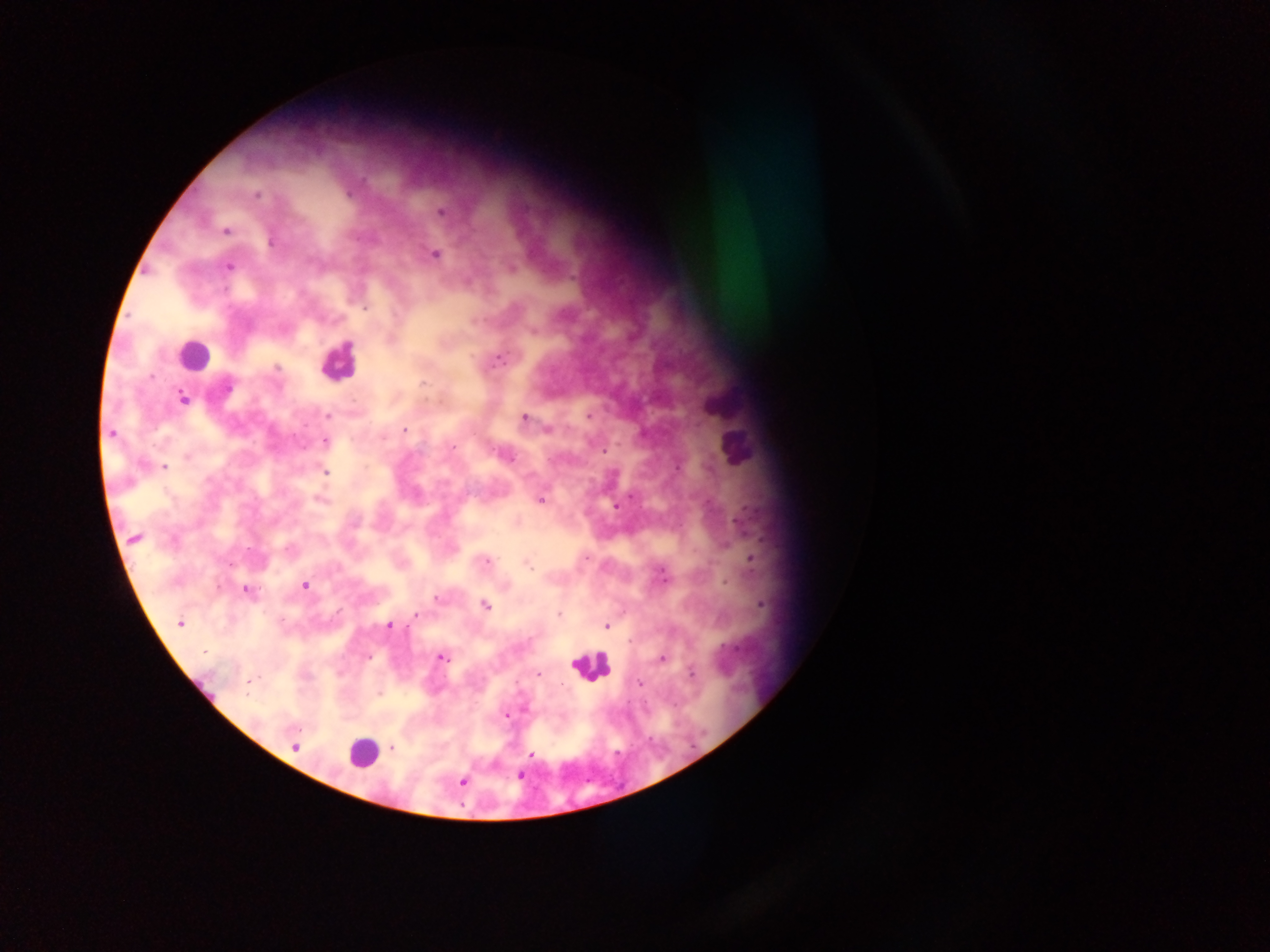

leukocyte_locations: 'approximate centers as (x, y) in pixels: (193, 355), (338, 362), (589, 665), (361, 754)'
country: Ghana
object_labeled_both_plasmodium_parasite_and_leukocyte_by_the_source: 'approximate centers as (x, y) in pixels: (735, 446)'
field_of_view: single
preparation: thick blood film
capture: mobile-phone photograph through a microscope
image_size: 1270×952 pixels
plasmodium_parasite_locations: 'approximate centers as (x, y) in pixels: (256, 195), (441, 212), (226, 231), (271, 242), (434, 254), (229, 267), (365, 308), (498, 359), (276, 367), (423, 383), (183, 399), (327, 415), (589, 416), (524, 417), (404, 430), (547, 430), (111, 434), (325, 442), (453, 447), (604, 451), (509, 458), (165, 466), (326, 473), (320, 500), (541, 500), (615, 505), (134, 539), (586, 557), (753, 560), (486, 561), (228, 564), (528, 567), (663, 576), (305, 586), (246, 590), (436, 598), (761, 604), (485, 605), (416, 615), (559, 615), (179, 624), (389, 625), (606, 627), (629, 641), (204, 652), (369, 657), (441, 658), (662, 659), (691, 674), (539, 675), (250, 681), (639, 683), (380, 694), (507, 715), (298, 730), (296, 747), (392, 748), (531, 755), (520, 776), (463, 782)'